State which cell type is depicted.
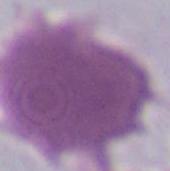

This is an erythrocyte.

Summary:
  - Magnification: 1000x
  - Modality: micrograph